Assess this cell for malaria.
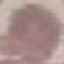
Uninfected.

capture: smartphone camera at the microscope eyepiece
preparation: thin blood film
image_type: cell patch, automatically extracted from a larger field of view and resized to 64 × 64 pixels
stain: Giemsa